Outline each Plasmodium ovale-infected red blood cell.
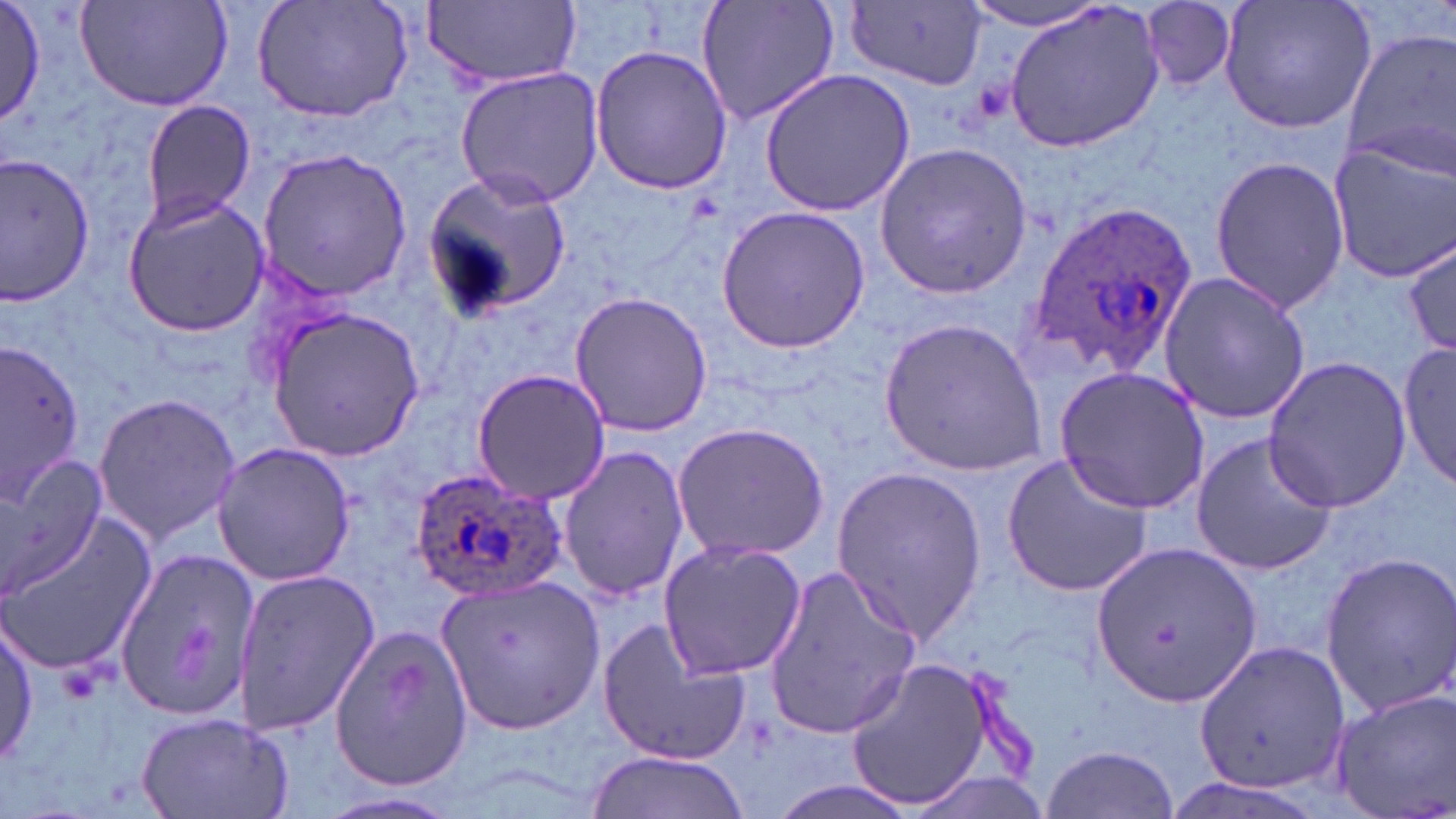
Approximate bounding boxes as (x1,y1)-(x2,y2) corner pairs in pixels.
Plasmodium ovale-infected red blood cells: (1022,200)-(1198,380), (407,464)-(570,609).

Uninfected red blood cell locations: (0,0)-(47,131), (253,0)-(414,125), (424,0)-(582,90), (695,0)-(842,127), (1003,0)-(1169,155), (1218,0)-(1378,134), (75,1)-(231,111), (846,2)-(990,89), (961,2)-(1113,33), (1140,2)-(1238,90), (1339,27)-(1456,181), (589,45)-(734,196), (454,67)-(606,207), (758,67)-(916,218), (136,99)-(257,227), (1326,140)-(1456,283), (875,141)-(1033,300), (258,148)-(412,299), (2,154)-(97,303), (1208,155)-(1351,313), (421,170)-(572,319), (121,193)-(271,336), (715,204)-(871,353), (1403,236)-(1455,360), (1157,268)-(1311,425), (568,292)-(715,438), (267,308)-(424,462), (879,318)-(1048,479), (1402,337)-(1454,493), (2,339)-(84,496), (1263,356)-(1411,515), (470,367)-(613,505), (1055,367)-(1212,512), (92,392)-(243,547), (671,421)-(830,564), (1190,429)-(1338,576), (211,440)-(357,587), (558,445)-(691,601), (0,449)-(113,594), (1000,450)-(1155,600), (831,464)-(988,644), (0,513)-(155,674), (656,539)-(808,683), (113,543)-(260,724), (1090,543)-(1262,713), (1320,552)-(1456,716), (762,563)-(922,740), (232,570)-(379,738), (438,575)-(605,733), (2,616)-(39,769), (596,617)-(750,765), (329,620)-(476,791), (1193,637)-(1352,797), (844,655)-(993,812), (1327,685)-(1456,819), (132,712)-(295,818), (1041,742)-(1179,815), (584,750)-(749,818), (899,770)-(1052,819), (766,777)-(926,819). Slide-level diagnosis: Plasmodium ovale. Image is 1456×819 pixels. 1000x magnification. May-Grünwald-Giemsa stain. Single field of view. Thin blood smear. Optical microscopy.